Point out each leukocyte.
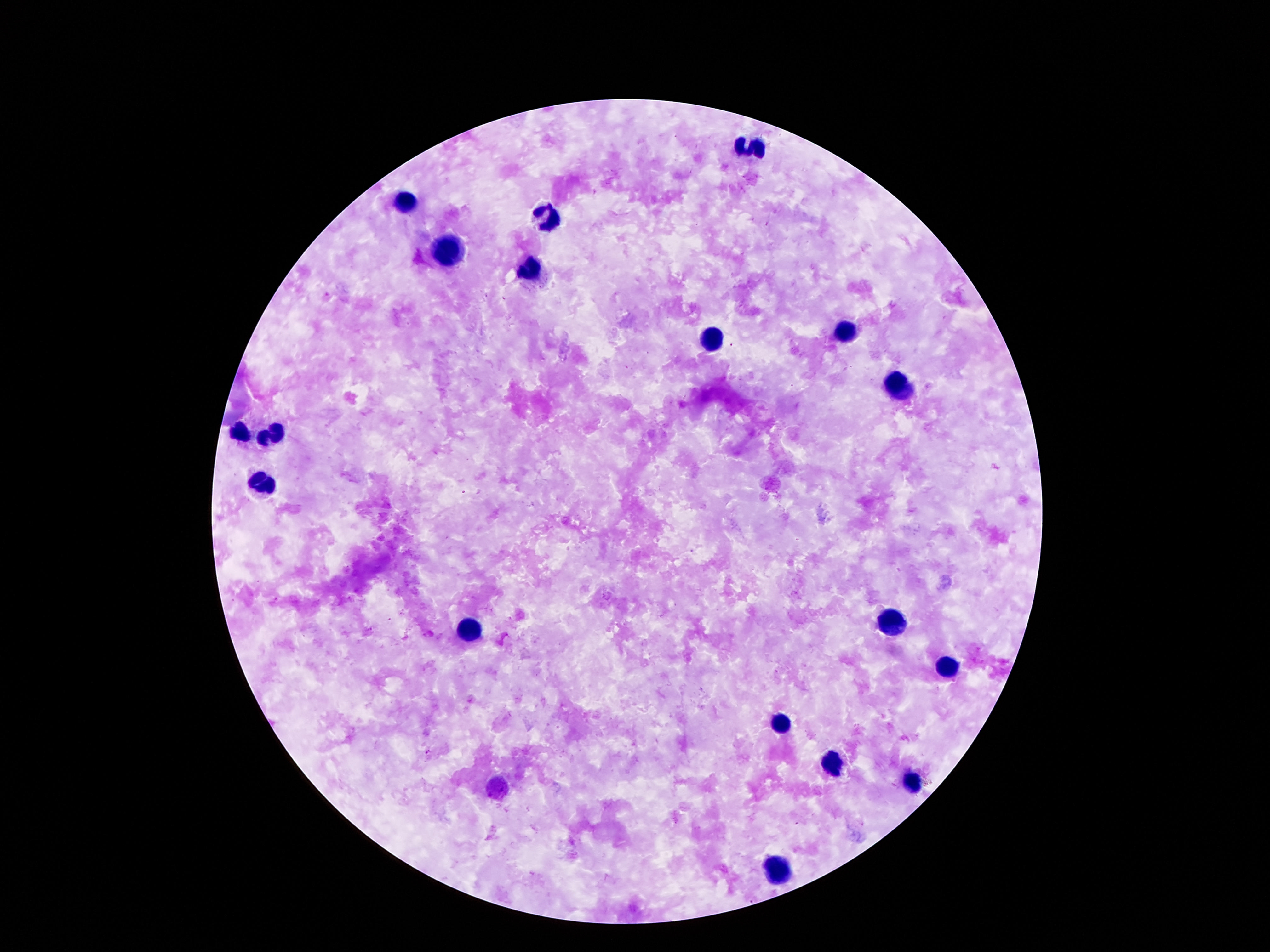

Approximate object centers, in pixels from the top-left corner.
Leukocytes: (x=753, y=146), (x=408, y=203), (x=549, y=217), (x=452, y=251), (x=531, y=271), (x=845, y=330), (x=710, y=336), (x=898, y=388), (x=241, y=433), (x=272, y=435), (x=258, y=482), (x=891, y=625), (x=473, y=631), (x=943, y=669), (x=784, y=722), (x=832, y=766), (x=914, y=783), (x=779, y=868).

{
  "field_of_view": "single",
  "image_size": "1270×952 pixels",
  "patient_malaria_status": "uninfected",
  "stain": "Giemsa",
  "preparation": "thick blood smear",
  "capture": "smartphone camera through the microscope eyepiece",
  "magnification": "100x"
}